Assess the morphology of the erythrocytes.
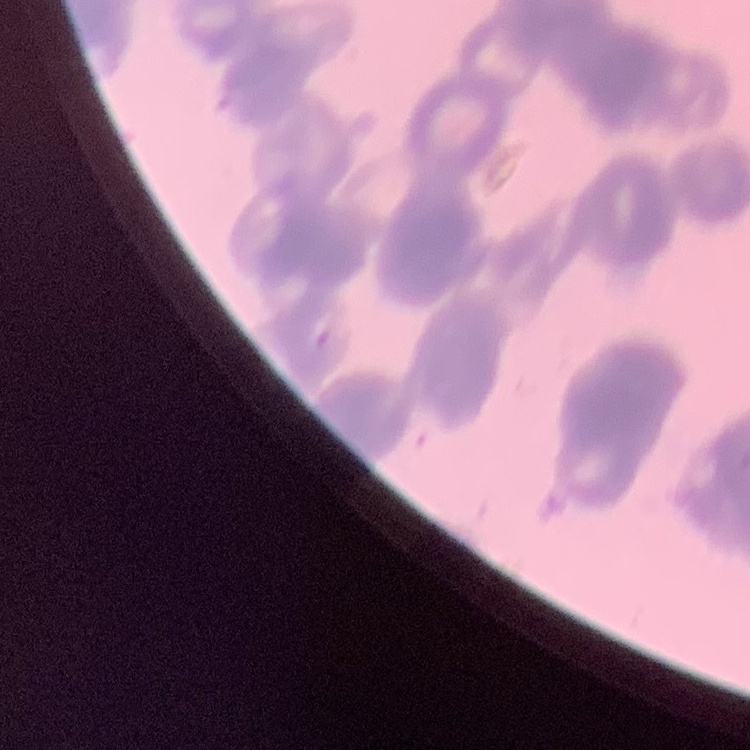
Rouleaux formation.

{
  "stain": "Field's or Giemsa",
  "image_type": "square crop of a larger photomicrograph",
  "preparation": "thin peripheral smear"
}